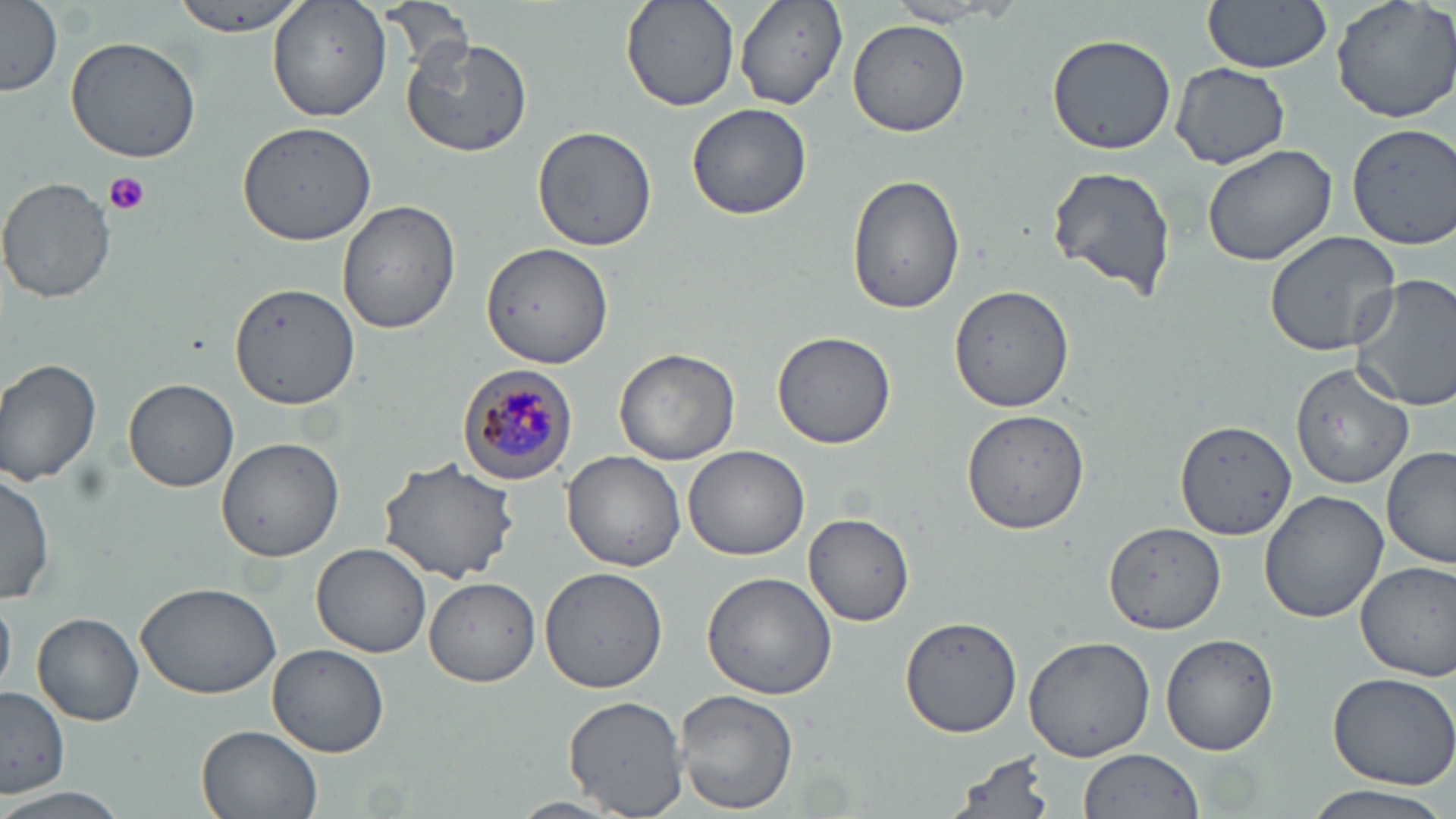

slide-level diagnosis = Plasmodium malariae
preparation = thin blood film
Plasmodium malariae-infected red blood cell locations = approximate bounding boxes as [x1, y1, x2, y2] in pixels: [457, 364, 578, 483]
image size = 1456×819 pixels
uninfected red blood cell locations = approximate bounding boxes as [x1, y1, x2, y2] in pixels: [167, 0, 313, 40], [267, 0, 392, 122], [622, 0, 740, 112], [736, 0, 849, 111], [1203, 0, 1332, 73], [1329, 0, 1456, 123], [0, 1, 63, 97], [883, 1, 1027, 29], [378, 4, 470, 71], [847, 20, 971, 137], [1046, 32, 1176, 156], [399, 35, 533, 158], [65, 36, 202, 164], [1170, 63, 1291, 168], [686, 103, 812, 220], [238, 120, 378, 247], [1346, 122, 1456, 248], [531, 126, 658, 251], [1199, 141, 1339, 267], [1045, 165, 1177, 301], [846, 171, 966, 316], [2, 178, 118, 301], [337, 201, 460, 335], [1263, 230, 1402, 356], [479, 242, 614, 368], [1349, 274, 1456, 412], [228, 281, 363, 410], [950, 283, 1073, 412], [772, 330, 897, 449], [614, 348, 740, 466], [0, 357, 101, 484], [1292, 360, 1414, 487], [123, 378, 239, 493], [961, 407, 1094, 536], [1173, 420, 1295, 541], [216, 437, 346, 563], [684, 445, 810, 560], [1379, 446, 1455, 569], [561, 450, 686, 572], [378, 458, 521, 583], [0, 470, 57, 604], [1258, 491, 1388, 622], [803, 512, 916, 626], [1103, 521, 1224, 637], [310, 543, 433, 658], [1354, 561, 1456, 681], [540, 566, 667, 693], [702, 570, 840, 700], [423, 577, 540, 686], [135, 579, 281, 698], [30, 610, 144, 727], [900, 614, 1023, 738], [1161, 633, 1282, 757], [1023, 635, 1155, 761], [265, 644, 389, 757], [1325, 671, 1456, 788], [1, 686, 70, 797], [673, 688, 799, 814], [563, 696, 688, 819], [196, 724, 326, 819], [1077, 749, 1203, 819], [942, 751, 1057, 819], [1299, 783, 1456, 817], [7, 789, 129, 819], [506, 796, 628, 818]
modality = optical microscopy
stain = May-Grünwald-Giemsa
magnification = 1000x
platelet locations = approximate bounding boxes as [x1, y1, x2, y2] in pixels: [102, 172, 152, 217]
field of view = single